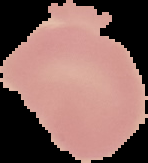

From a thin blood smear. Image is 148×163 pixels. Malaria status: uninfected. Cell region segmented out of the field of view; the surrounding area is masked to black.